Outline each uninfected red blood cell.
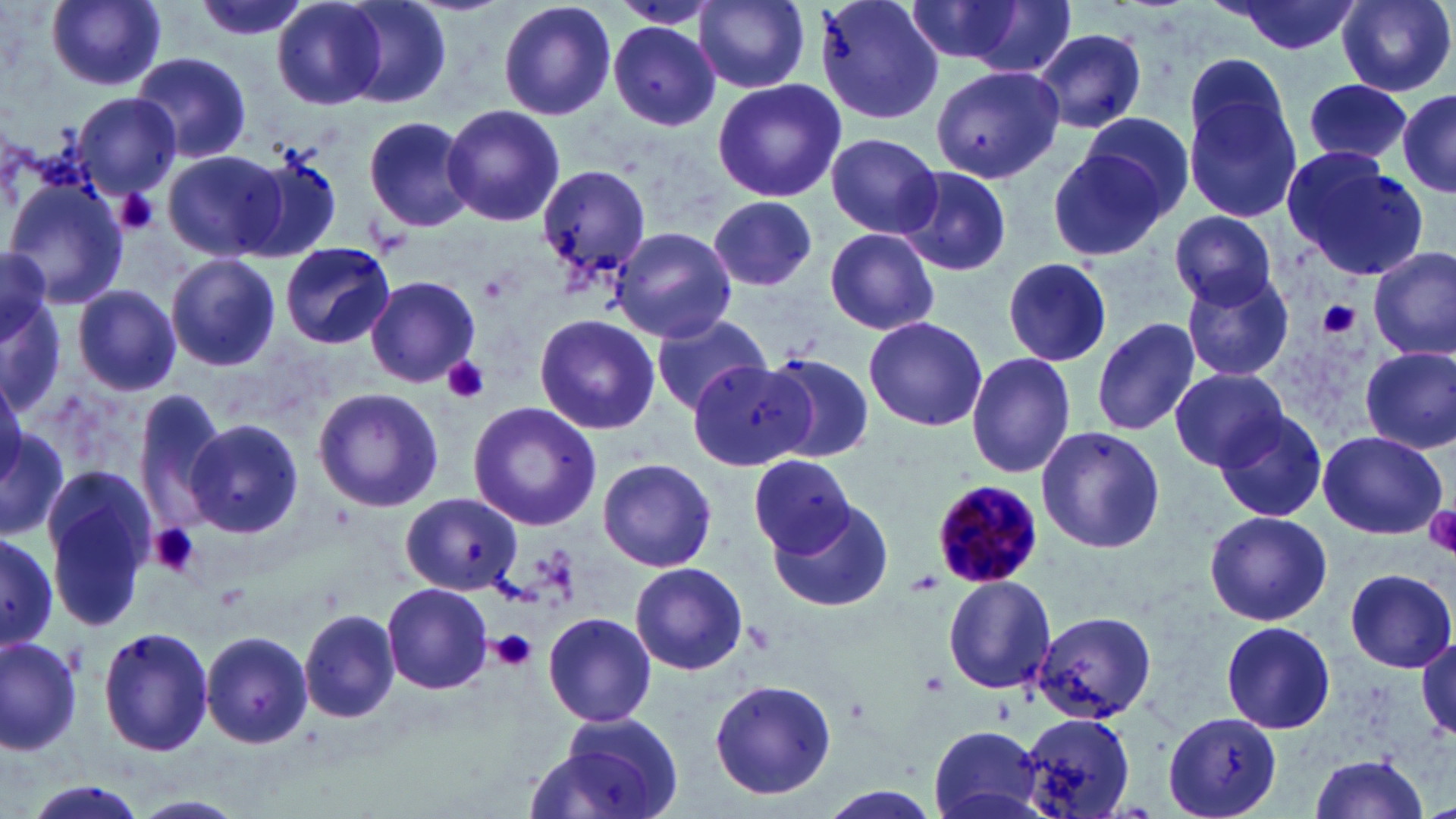

Approximate bounding boxes as (x1,y1)-(x2,y2) corner pairs in pixels.
Uninfected red blood cells (subset): (44,0)-(169,90), (191,0)-(308,44), (694,0)-(811,92), (815,0)-(946,126), (1218,0)-(1361,54), (1337,0)-(1454,96), (495,1)-(616,120), (612,1)-(718,29), (912,1)-(1078,76), (270,2)-(388,110), (336,2)-(452,110), (608,22)-(721,132), (1030,27)-(1148,133), (130,51)-(251,165), (924,62)-(1065,187), (1180,64)-(1303,225), (1300,77)-(1418,173), (710,79)-(846,204), (1395,89)-(1455,200), (72,93)-(179,200), (443,104)-(564,227), (1075,112)-(1198,224), (364,116)-(478,234), (825,132)-(944,239), (1043,142)-(1175,264), (238,149)-(344,263), (1280,149)-(1427,279), (165,150)-(289,260), (536,163)-(650,288), (897,165)-(1012,277), (6,177)-(129,308), (710,198)-(818,293), (1170,211)-(1278,309), (612,227)-(737,344), (823,228)-(940,336), (279,242)-(395,349), (1368,246)-(1455,364), (0,247)-(53,355), (166,254)-(282,371), (999,257)-(1113,366), (1180,270)-(1295,384), (365,276)-(480,387), (1,284)-(64,414), (74,285)-(181,396), (651,313)-(772,415), (533,314)-(660,435), (863,316)-(988,430), (1091,316)-(1200,436), (1359,346)-(1455,453), (964,353)-(1077,479), (762,354)-(875,464), (686,361)-(809,472), (1170,368)-(1289,471), (134,387)-(226,530), (314,388)-(444,512), (468,400)-(601,533), (1215,409)-(1326,522), (186,420)-(304,540), (0,422)-(68,539), (1036,427)-(1166,554), (1317,430)-(1447,540), (749,455)-(854,556), (596,458)-(718,572), (45,465)-(155,631), (402,492)-(522,595), (772,498)-(894,613), (1204,510)-(1333,624), (0,531)-(59,649), (629,562)-(747,676), (1343,568)-(1455,673), (941,575)-(1056,696), (382,581)-(493,695), (300,609)-(399,722), (1028,609)-(1160,723), (543,611)-(658,728), (1219,620)-(1336,736), (97,625)-(215,757), (201,631)-(315,750), (1413,632)-(1456,741), (0,634)-(85,756), (706,680)-(837,801), (1164,710)-(1285,819), (1020,711)-(1137,817), (542,713)-(685,819), (925,726)-(1049,819), (1303,755)-(1432,819), (16,779)-(152,819), (815,786)-(944,819), (128,792)-(248,819).

Summary:
  - Platelet locations: (116,191)-(160,235), (1319,300)-(1360,338), (441,356)-(490,404), (1423,504)-(1456,558), (149,522)-(201,577), (910,570)-(943,595), (492,629)-(538,674), (918,670)-(950,698)
  - Slide-level diagnosis: Plasmodium malariae
  - Modality: light microscopy
  - Field of view: one of a larger specimen
  - Preparation: thin blood film
  - Image size: 1456×819 pixels
  - Magnification: 1000x
  - Stain: May-Grünwald-Giemsa